Assess this cell for malaria.
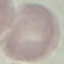
Uninfected.

Summary:
  - Stain: Giemsa
  - Capture: smartphone through the microscope eyepiece
  - Preparation: thin blood film
  - Image type: cell patch, automatically extracted from a larger field of view and resized to 64 × 64 pixels